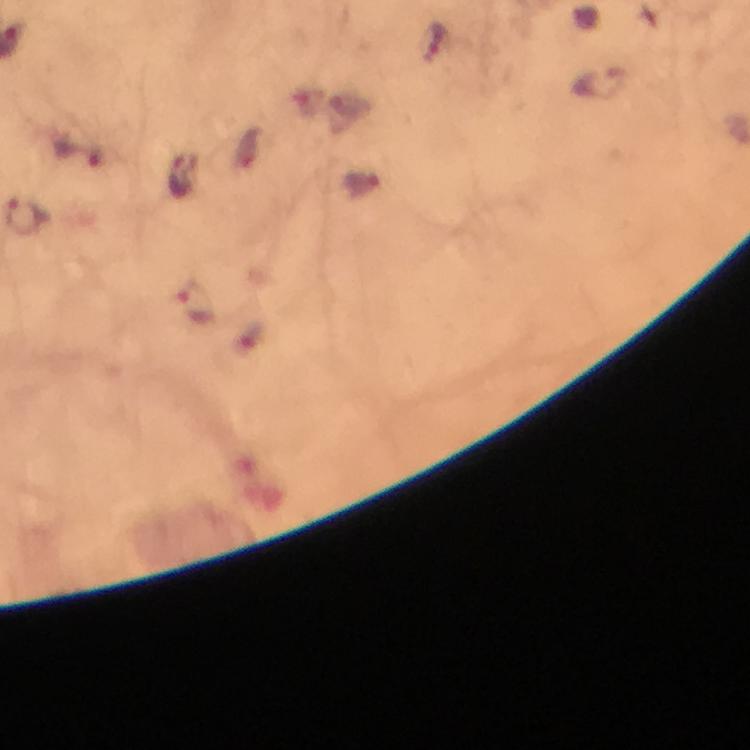

magnification = 100x
malaria parasite locations = approximate centers as (x, y) in pixels: (434, 43), (598, 82), (25, 219), (195, 304)
capture = smartphone photograph through a microscope
immersion oil = used
image size = 750×750 pixels
stain = Giemsa
context = from a malaria diagnostic workup
cropped from = one field of view
preparation = thick smear